Identify the parasite.
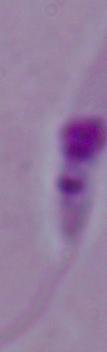
This is Leishmania.

magnification: 1000x
modality: micrograph